Report the malaria status of this cell.
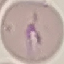
It is parasitized.

Cell patch, automatically extracted from a larger field of view and resized to 64 × 64 pixels. Giemsa-stained preparation. Thin blood smear. Photographed with a smartphone camera at the microscope eyepiece.